Report the malaria status of this cell.
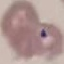
Uninfected.

Giemsa stain. Cell patch, automatically extracted from a larger field of view and resized to 64 × 64 pixels. Thin blood smear. Photographed with a smartphone camera at the microscope eyepiece.